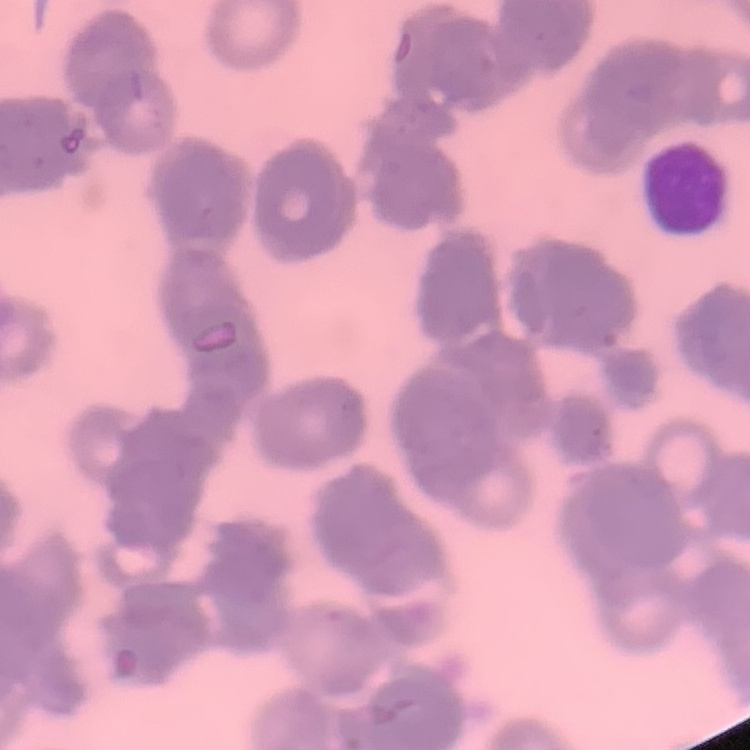

Summary:
  - Erythrocyte morphology: rouleaux formation
  - Image type: square crop of a larger photomicrograph
  - Stain: Field's or Giemsa
  - Preparation: thin blood smear